Find each parasitized red blood cell.
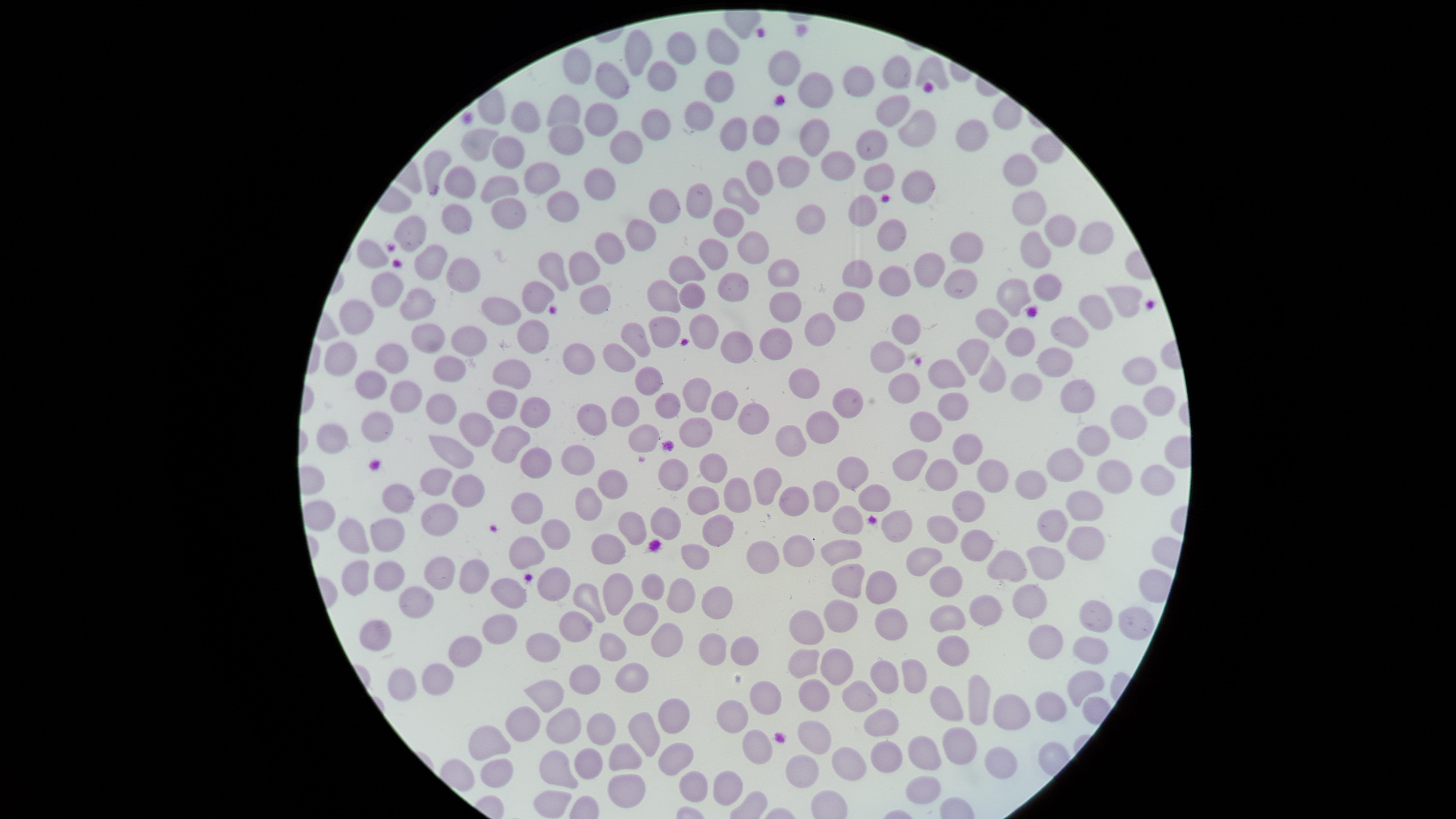

No parasitized red blood cells identified.

Approximate bounding boxes, in pixels from the top-left corner. Uninfected red blood cells: (left=706, top=27, right=740, bottom=65), (left=624, top=29, right=652, bottom=77), (left=667, top=31, right=697, bottom=66), (left=562, top=48, right=592, bottom=85), (left=768, top=50, right=801, bottom=86), (left=882, top=55, right=912, bottom=89), (left=916, top=55, right=949, bottom=90), (left=647, top=59, right=677, bottom=92), (left=595, top=61, right=629, bottom=99), (left=843, top=65, right=875, bottom=98), (left=704, top=70, right=734, bottom=103), (left=798, top=72, right=834, bottom=108), (left=547, top=94, right=581, bottom=126), (left=875, top=95, right=911, bottom=127), (left=511, top=101, right=541, bottom=133), (left=684, top=101, right=714, bottom=131), (left=585, top=103, right=618, bottom=137), (left=641, top=108, right=671, bottom=141), (left=897, top=109, right=937, bottom=147), (left=753, top=114, right=781, bottom=145), (left=720, top=117, right=748, bottom=152), (left=799, top=118, right=831, bottom=157), (left=955, top=119, right=989, bottom=152), (left=548, top=124, right=584, bottom=155), (left=460, top=128, right=498, bottom=161), (left=856, top=128, right=888, bottom=161), (left=610, top=129, right=643, bottom=163), (left=1031, top=135, right=1064, bottom=163), (left=492, top=136, right=524, bottom=169), (left=424, top=151, right=452, bottom=196), (left=820, top=151, right=857, bottom=181), (left=1003, top=153, right=1038, bottom=186), (left=777, top=156, right=811, bottom=187), (left=746, top=160, right=774, bottom=196), (left=524, top=162, right=560, bottom=194), (left=863, top=162, right=895, bottom=192), (left=444, top=166, right=475, bottom=199), (left=584, top=168, right=615, bottom=200), (left=902, top=170, right=935, bottom=204), (left=481, top=176, right=519, bottom=204), (left=723, top=177, right=760, bottom=214), (left=686, top=183, right=713, bottom=218), (left=649, top=188, right=681, bottom=223), (left=1012, top=190, right=1047, bottom=225), (left=546, top=191, right=579, bottom=223), (left=849, top=194, right=878, bottom=225), (left=492, top=198, right=527, bottom=230), (left=441, top=204, right=472, bottom=235), (left=796, top=204, right=826, bottom=234), (left=713, top=207, right=745, bottom=237), (left=1044, top=215, right=1077, bottom=247), (left=393, top=216, right=426, bottom=252), (left=625, top=218, right=657, bottom=251), (left=878, top=219, right=907, bottom=251), (left=1078, top=222, right=1114, bottom=255), (left=737, top=231, right=770, bottom=263), (left=1020, top=231, right=1052, bottom=269), (left=951, top=232, right=984, bottom=264), (left=596, top=233, right=625, bottom=264), (left=698, top=238, right=728, bottom=270), (left=357, top=239, right=389, bottom=269), (left=414, top=244, right=448, bottom=280), (left=569, top=251, right=599, bottom=286), (left=537, top=252, right=569, bottom=291), (left=913, top=252, right=946, bottom=288), (left=669, top=255, right=704, bottom=285), (left=446, top=258, right=480, bottom=293), (left=767, top=259, right=799, bottom=287), (left=842, top=259, right=873, bottom=289), (left=879, top=265, right=912, bottom=297), (left=943, top=268, right=978, bottom=299), (left=371, top=272, right=403, bottom=306), (left=717, top=272, right=749, bottom=301), (left=1033, top=273, right=1062, bottom=301), (left=996, top=278, right=1031, bottom=317), (left=647, top=279, right=680, bottom=313), (left=521, top=281, right=554, bottom=314), (left=679, top=283, right=705, bottom=309), (left=579, top=285, right=611, bottom=315), (left=1107, top=286, right=1142, bottom=318), (left=400, top=289, right=436, bottom=319), (left=769, top=291, right=802, bottom=323), (left=832, top=292, right=865, bottom=322), (left=1079, top=295, right=1113, bottom=330), (left=481, top=297, right=522, bottom=325), (left=339, top=299, right=374, bottom=335), (left=975, top=308, right=1008, bottom=338), (left=804, top=312, right=835, bottom=346), (left=688, top=313, right=719, bottom=350), (left=891, top=314, right=920, bottom=346), (left=649, top=316, right=680, bottom=348), (left=1050, top=317, right=1088, bottom=348), (left=516, top=320, right=549, bottom=354), (left=621, top=323, right=651, bottom=357), (left=411, top=324, right=444, bottom=354), (left=451, top=326, right=487, bottom=357), (left=759, top=328, right=793, bottom=360), (left=1005, top=328, right=1035, bottom=357), (left=720, top=330, right=753, bottom=363), (left=957, top=338, right=990, bottom=375), (left=870, top=340, right=905, bottom=374), (left=325, top=342, right=357, bottom=375), (left=376, top=343, right=408, bottom=373), (left=563, top=343, right=595, bottom=375), (left=603, top=343, right=635, bottom=372), (left=1037, top=347, right=1073, bottom=377), (left=979, top=355, right=1006, bottom=393), (left=434, top=356, right=465, bottom=382), (left=1121, top=356, right=1157, bottom=385), (left=928, top=359, right=965, bottom=390), (left=491, top=360, right=531, bottom=389), (left=635, top=366, right=663, bottom=395), (left=789, top=368, right=820, bottom=399), (left=356, top=371, right=387, bottom=400), (left=888, top=373, right=920, bottom=404), (left=1011, top=373, right=1042, bottom=402), (left=683, top=378, right=712, bottom=413), (left=1060, top=379, right=1095, bottom=413), (left=390, top=381, right=422, bottom=413), (left=1143, top=385, right=1176, bottom=417), (left=832, top=388, right=864, bottom=418), (left=487, top=390, right=517, bottom=419), (left=711, top=391, right=738, bottom=420), (left=654, top=392, right=681, bottom=419), (left=938, top=392, right=969, bottom=422), (left=425, top=393, right=456, bottom=425), (left=611, top=395, right=640, bottom=427), (left=520, top=396, right=551, bottom=428), (left=576, top=403, right=607, bottom=436), (left=738, top=403, right=770, bottom=434), (left=1110, top=405, right=1147, bottom=440), (left=806, top=411, right=840, bottom=444), (left=361, top=412, right=394, bottom=442), (left=458, top=412, right=493, bottom=446), (left=909, top=412, right=942, bottom=443), (left=678, top=417, right=713, bottom=447), (left=316, top=424, right=348, bottom=454), (left=628, top=424, right=660, bottom=453), (left=775, top=425, right=806, bottom=457), (left=1077, top=425, right=1110, bottom=456), (left=491, top=426, right=530, bottom=464), (left=953, top=433, right=982, bottom=466), (left=429, top=435, right=473, bottom=469), (left=560, top=444, right=595, bottom=476), (left=520, top=447, right=552, bottom=479), (left=1047, top=447, right=1083, bottom=482), (left=893, top=449, right=927, bottom=481), (left=699, top=453, right=727, bottom=483), (left=837, top=456, right=869, bottom=490), (left=658, top=459, right=689, bottom=491), (left=977, top=459, right=1009, bottom=493), (left=1097, top=459, right=1132, bottom=494), (left=925, top=460, right=958, bottom=492), (left=1141, top=464, right=1175, bottom=496), (left=420, top=468, right=452, bottom=496), (left=597, top=468, right=627, bottom=499), (left=754, top=468, right=782, bottom=505), (left=1015, top=470, right=1047, bottom=500), (left=451, top=474, right=485, bottom=507), (left=723, top=477, right=752, bottom=513), (left=812, top=481, right=840, bottom=513), (left=382, top=484, right=414, bottom=514), (left=858, top=484, right=890, bottom=512), (left=688, top=485, right=720, bottom=515), (left=779, top=486, right=809, bottom=516), (left=574, top=487, right=602, bottom=521), (left=951, top=490, right=985, bottom=522), (left=1066, top=490, right=1103, bottom=522), (left=511, top=492, right=543, bottom=524), (left=421, top=504, right=459, bottom=536), (left=832, top=505, right=864, bottom=535), (left=650, top=507, right=681, bottom=541), (left=1037, top=509, right=1068, bottom=542), (left=881, top=510, right=912, bottom=542), (left=618, top=511, right=647, bottom=545), (left=702, top=515, right=734, bottom=547), (left=927, top=515, right=958, bottom=544), (left=338, top=518, right=370, bottom=554), (left=370, top=518, right=404, bottom=552), (left=541, top=519, right=570, bottom=550), (left=1067, top=527, right=1105, bottom=561), (left=961, top=529, right=993, bottom=562), (left=591, top=533, right=626, bottom=564), (left=782, top=535, right=815, bottom=567), (left=509, top=536, right=545, bottom=570), (left=746, top=540, right=779, bottom=574), (left=819, top=540, right=863, bottom=566), (left=681, top=544, right=710, bottom=570), (left=1026, top=545, right=1065, bottom=580), (left=906, top=547, right=943, bottom=576), (left=986, top=550, right=1027, bottom=582), (left=424, top=555, right=455, bottom=590), (left=459, top=559, right=489, bottom=594), (left=342, top=560, right=369, bottom=595), (left=374, top=561, right=405, bottom=591), (left=832, top=563, right=864, bottom=599), (left=537, top=566, right=571, bottom=601), (left=930, top=566, right=963, bottom=598), (left=865, top=570, right=897, bottom=604), (left=602, top=573, right=634, bottom=616), (left=641, top=573, right=665, bottom=600), (left=492, top=577, right=527, bottom=609), (left=667, top=579, right=696, bottom=613), (left=572, top=583, right=606, bottom=623), (left=1012, top=584, right=1047, bottom=618), (left=701, top=585, right=734, bottom=618), (left=398, top=586, right=433, bottom=619), (left=968, top=594, right=1001, bottom=626), (left=1079, top=599, right=1113, bottom=633), (left=823, top=600, right=858, bottom=633), (left=624, top=602, right=659, bottom=637), (left=930, top=605, right=966, bottom=633), (left=1118, top=607, right=1154, bottom=641), (left=875, top=608, right=907, bottom=640), (left=789, top=610, right=824, bottom=644), (left=559, top=611, right=593, bottom=642), (left=483, top=614, right=518, bottom=644), (left=359, top=619, right=392, bottom=651), (left=651, top=622, right=683, bottom=658), (left=1029, top=623, right=1063, bottom=660), (left=599, top=631, right=626, bottom=661), (left=525, top=633, right=561, bottom=662), (left=699, top=634, right=727, bottom=666), (left=936, top=635, right=969, bottom=667), (left=448, top=636, right=483, bottom=668), (left=731, top=636, right=760, bottom=666), (left=1073, top=637, right=1109, bottom=665), (left=821, top=648, right=853, bottom=685), (left=787, top=649, right=820, bottom=679), (left=901, top=658, right=926, bottom=693), (left=869, top=661, right=898, bottom=693), (left=422, top=663, right=454, bottom=697), (left=615, top=663, right=649, bottom=693), (left=570, top=665, right=601, bottom=695), (left=388, top=668, right=417, bottom=701), (left=1068, top=670, right=1105, bottom=706), (left=968, top=674, right=991, bottom=726), (left=799, top=678, right=830, bottom=712), (left=526, top=680, right=565, bottom=712), (left=842, top=680, right=878, bottom=712), (left=750, top=681, right=782, bottom=715), (left=929, top=685, right=963, bottom=720), (left=1035, top=691, right=1066, bottom=721), (left=993, top=694, right=1031, bottom=730), (left=658, top=697, right=690, bottom=733), (left=717, top=699, right=748, bottom=733), (left=506, top=706, right=541, bottom=742), (left=547, top=707, right=582, bottom=744), (left=864, top=708, right=899, bottom=737), (left=586, top=712, right=617, bottom=746), (left=629, top=712, right=660, bottom=757), (left=797, top=721, right=831, bottom=754), (left=469, top=725, right=511, bottom=761), (left=942, top=727, right=977, bottom=765), (left=742, top=729, right=772, bottom=764), (left=907, top=736, right=941, bottom=770), (left=658, top=741, right=695, bottom=775), (left=871, top=741, right=903, bottom=773), (left=609, top=742, right=643, bottom=771), (left=832, top=747, right=867, bottom=780), (left=984, top=747, right=1018, bottom=779), (left=574, top=748, right=604, bottom=779), (left=540, top=750, right=579, bottom=789), (left=785, top=755, right=819, bottom=788), (left=480, top=758, right=514, bottom=787), (left=713, top=769, right=743, bottom=805), (left=680, top=771, right=709, bottom=802), (left=608, top=774, right=647, bottom=808), (left=906, top=775, right=940, bottom=804). Thin blood film. Smartphone photograph through the microscope eyepiece. Image is 1456×819 pixels. One field of view of the specimen. The visible region is circular. Giemsa stain.